Locate every blood parasite and identify its species.
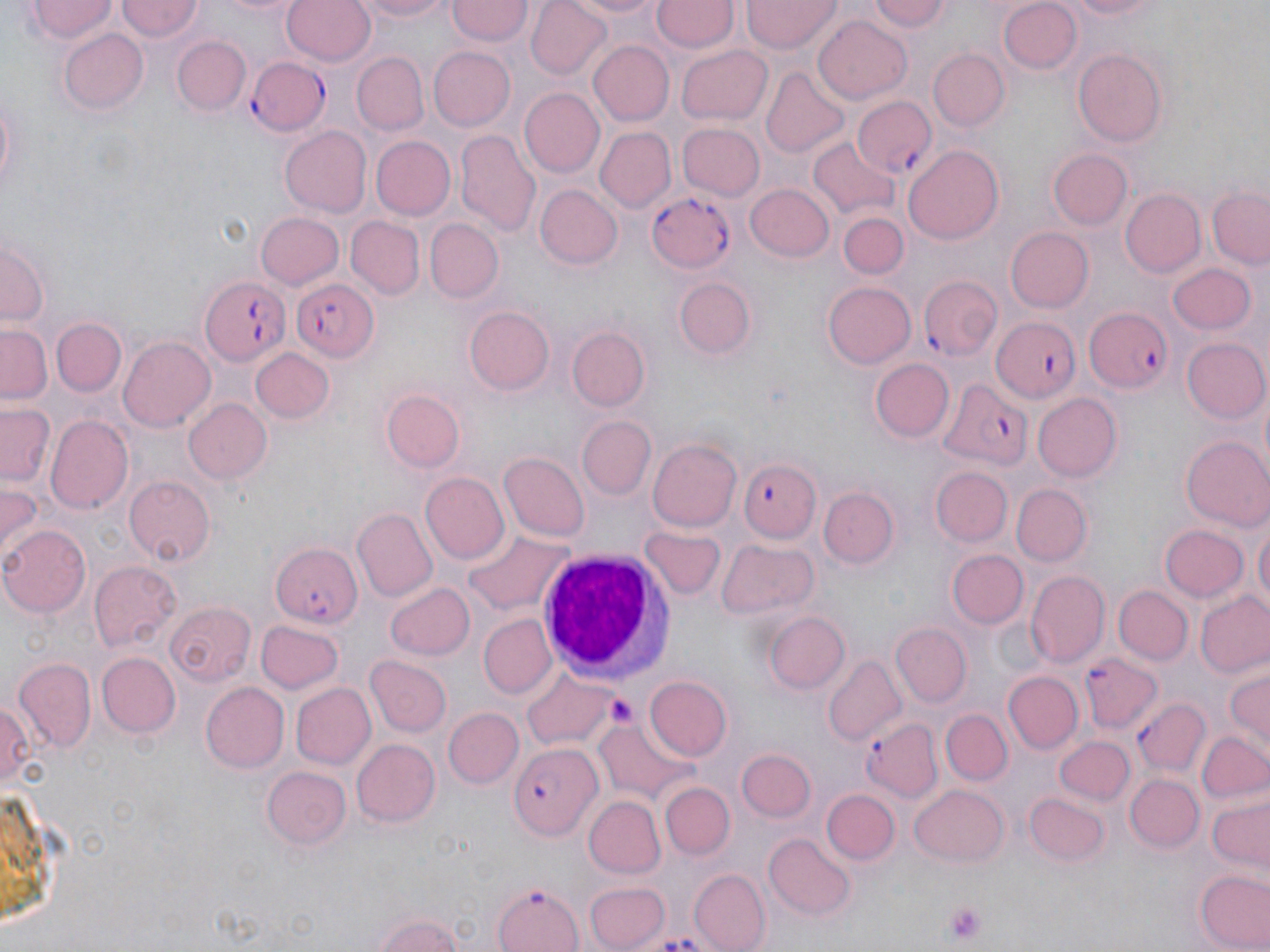
Approximate bounding boxes as [x1, y1, x2, y2] in pixels.
Plasmodium falciparum-infected red blood cells: [248, 58, 329, 137], [853, 96, 937, 178], [647, 189, 739, 271], [200, 277, 291, 367], [293, 278, 380, 361], [919, 278, 1001, 360], [1085, 304, 1179, 396], [991, 317, 1082, 404], [935, 378, 1033, 469], [740, 460, 822, 542], [272, 541, 364, 629], [1080, 653, 1159, 732], [1132, 697, 1207, 778], [859, 717, 944, 803], [510, 744, 603, 838], [491, 881, 586, 952].
No Plasmodium ovale, Plasmodium malariae, Plasmodium vivax, Babesia divergens, or Trypanosoma brucei observed.

slide-level diagnosis = Plasmodium falciparum
field of view = one of a larger specimen
stain = May-Grünwald-Giemsa
platelet locations = approximate bounding boxes as [x1, y1, x2, y2] in pixels: [603, 694, 636, 726], [941, 900, 987, 943]
image size = 1270×952 pixels
uninfected red blood cell locations = approximate bounding boxes as [x1, y1, x2, y2] in pixels: [115, 0, 204, 42], [216, 0, 307, 19], [282, 0, 375, 67], [353, 0, 457, 23], [525, 0, 612, 78], [558, 0, 671, 21], [653, 0, 736, 52], [741, 0, 840, 53], [867, 0, 953, 36], [1062, 0, 1169, 21], [27, 1, 117, 44], [999, 1, 1082, 74], [445, 2, 532, 47], [814, 15, 912, 104], [60, 28, 147, 114], [173, 36, 248, 117], [589, 41, 673, 124], [676, 44, 773, 124], [426, 46, 515, 131], [1073, 49, 1168, 147], [929, 50, 1009, 131], [350, 52, 429, 135], [761, 67, 849, 158], [0, 87, 22, 203], [519, 88, 605, 178], [677, 124, 765, 202], [278, 126, 372, 218], [595, 128, 675, 212], [456, 134, 540, 238], [372, 135, 455, 219], [809, 139, 896, 222], [904, 144, 1004, 243], [1047, 149, 1131, 230], [534, 184, 623, 269], [744, 184, 833, 263], [1209, 188, 1269, 269], [1120, 190, 1207, 278], [255, 211, 345, 291], [840, 213, 907, 277], [348, 217, 423, 298], [426, 220, 503, 301], [1006, 227, 1094, 311], [1, 241, 47, 328], [1167, 263, 1258, 335], [676, 274, 758, 360], [822, 282, 915, 369], [461, 303, 555, 399], [51, 318, 126, 396], [0, 321, 52, 402], [567, 328, 650, 412], [118, 336, 215, 430], [1184, 339, 1269, 424], [251, 348, 336, 424], [870, 357, 954, 442], [381, 391, 463, 472], [1031, 391, 1121, 482], [183, 399, 272, 485], [2, 403, 56, 489], [46, 416, 133, 515], [576, 417, 655, 500], [1182, 437, 1270, 534], [646, 438, 742, 533], [499, 453, 590, 542], [931, 467, 1013, 547], [421, 473, 510, 565], [123, 476, 214, 566], [0, 483, 43, 566], [1012, 484, 1092, 565], [820, 485, 899, 569], [352, 510, 436, 600], [1253, 519, 1268, 617], [1, 524, 91, 617], [1160, 524, 1248, 602], [463, 526, 574, 616], [640, 527, 726, 602], [719, 541, 819, 619], [948, 549, 1026, 628], [89, 561, 180, 650], [1026, 572, 1110, 665], [386, 583, 475, 661], [1115, 586, 1191, 664], [1194, 590, 1270, 678], [167, 601, 255, 684], [762, 611, 849, 694], [481, 616, 556, 696], [253, 620, 344, 695], [889, 624, 971, 706], [95, 653, 179, 737], [367, 655, 452, 737], [824, 656, 905, 744], [13, 660, 95, 752], [1224, 666, 1269, 751], [519, 669, 616, 750], [1002, 671, 1082, 753], [644, 676, 733, 762], [290, 682, 376, 770], [200, 683, 289, 773], [0, 699, 35, 794], [443, 707, 523, 787], [941, 710, 1012, 785], [594, 718, 697, 804], [1197, 732, 1270, 807], [1053, 736, 1133, 804], [352, 738, 438, 827], [737, 750, 815, 821], [262, 766, 351, 850], [1126, 775, 1204, 852], [0, 777, 53, 927], [659, 782, 734, 858], [909, 784, 1009, 868], [823, 789, 899, 867], [1027, 794, 1111, 866], [1206, 795, 1268, 872], [584, 797, 667, 879], [766, 833, 856, 919], [1193, 867, 1269, 952], [686, 869, 769, 952], [583, 881, 672, 951], [367, 910, 473, 952]
white blood cell locations = approximate bounding boxes as [x1, y1, x2, y2] in pixels: [537, 548, 671, 681]
modality = optical microscopy
magnification = 1000x
preparation = thin blood film